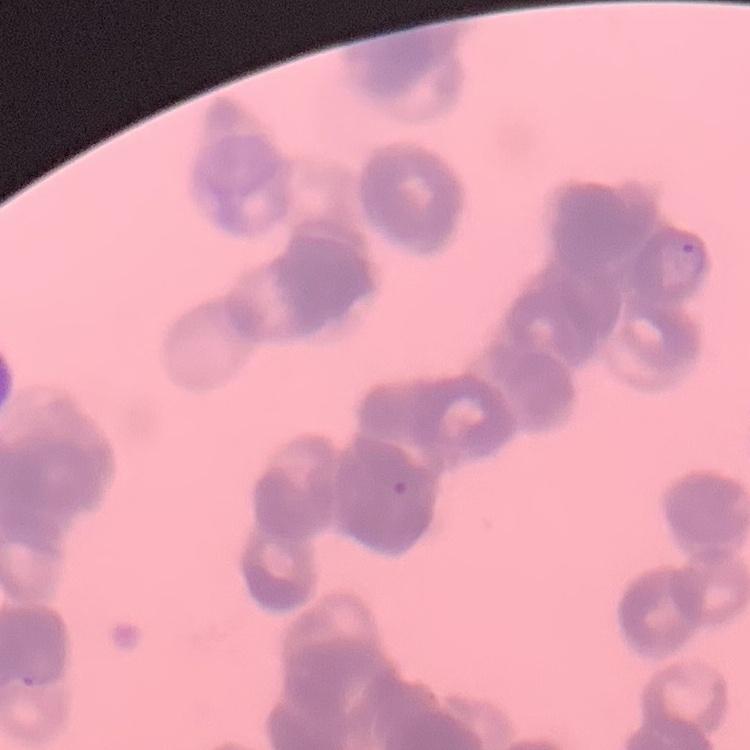

erythrocyte morphology = rouleaux formation
image type = square crop of a larger photomicrograph
preparation = thin peripheral smear
stain = Field's or Giemsa